Report the malaria status of this cell.
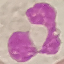

Uninfected.

preparation = thin blood smear
image type = cell patch, automatically extracted from a larger field of view and resized to 64 × 64 pixels
stain = Giemsa
capture = smartphone camera at the microscope eyepiece